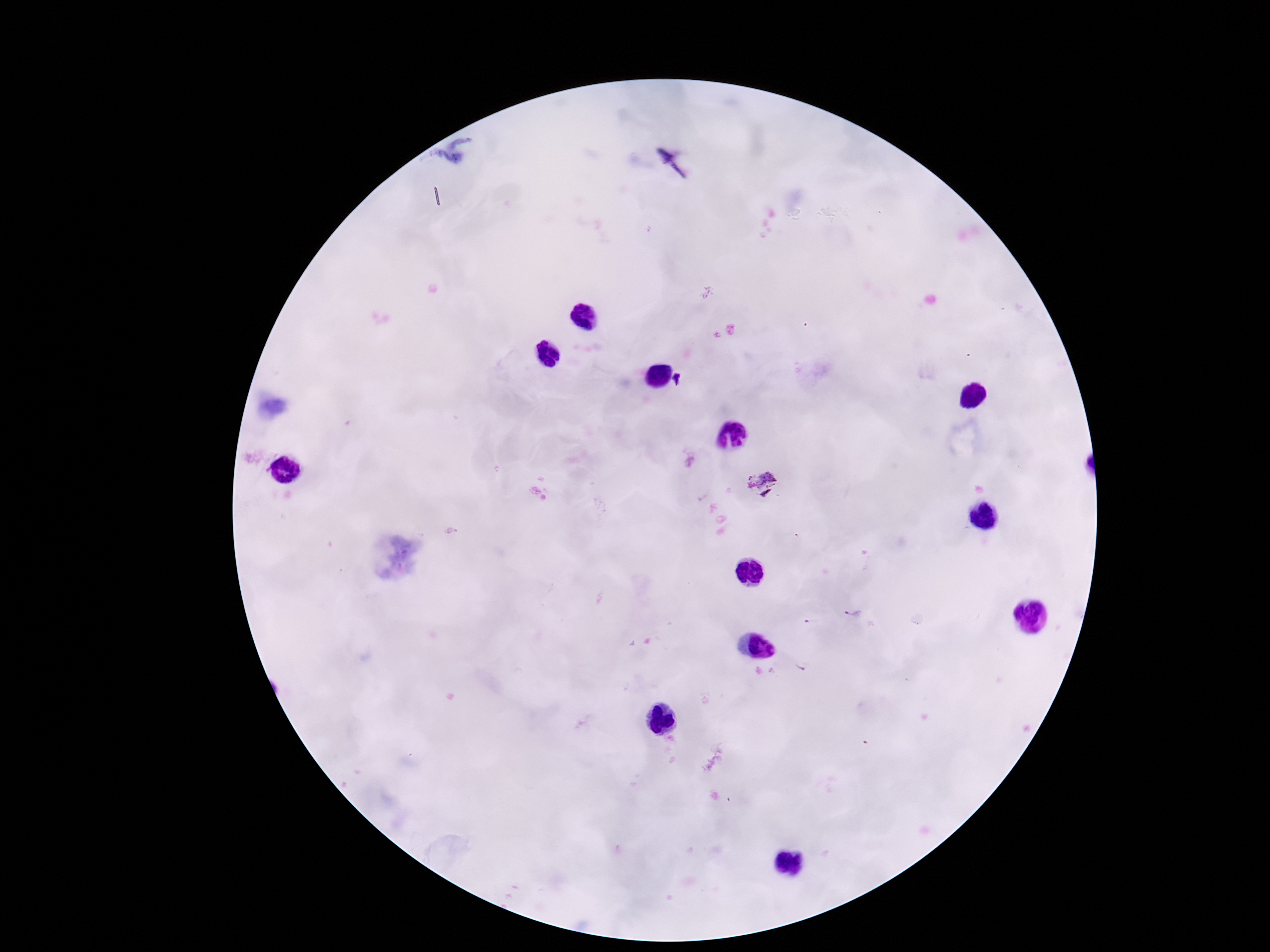

Approximate centers as [x, y] in pixels. Plasmodium parasite locations: [679, 380], [762, 486], [851, 613], [808, 623], [801, 666]. Smartphone photograph taken through the microscope eyepiece. Single field of view. Thick blood smear. Image is 1270×952 pixels. Giemsa-stained preparation. Patient malaria status: positive. 100x magnification.